Assess this cell for malaria.
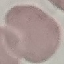

Uninfected.

preparation = thin blood film
capture = smartphone camera at the microscope eyepiece
stain = Giemsa
image type = cell patch, automatically extracted from a larger field of view and resized to 64 × 64 pixels